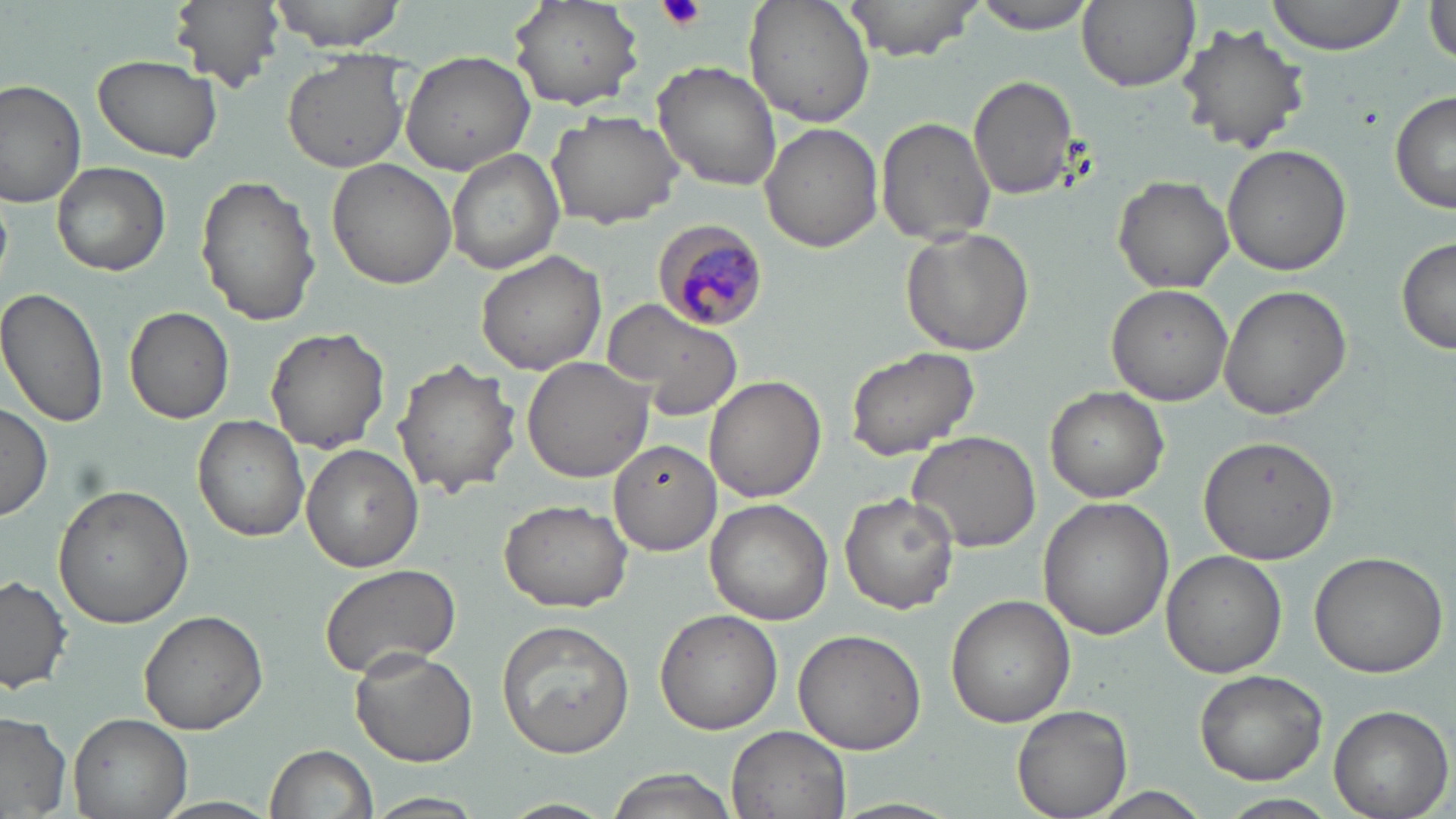

slide_level_diagnosis: Plasmodium malariae
stain: May-Grünwald-Giemsa
uninfected_red_blood_cell_locations: 'approximate bounding boxes as (x1, y1, x2, y2) in pixels: (171, 0, 285, 92), (266, 0, 413, 51), (510, 0, 645, 112), (742, 0, 876, 127), (841, 0, 987, 62), (969, 0, 1102, 35), (1077, 0, 1200, 92), (1265, 0, 1411, 55), (1424, 5, 1456, 66), (1176, 21, 1311, 152), (399, 48, 538, 175), (281, 49, 413, 173), (92, 53, 223, 162), (652, 61, 783, 191), (969, 74, 1081, 202), (0, 78, 89, 210), (1390, 90, 1456, 214), (545, 109, 683, 229), (875, 115, 996, 248), (760, 123, 884, 252), (1220, 145, 1353, 276), (445, 149, 564, 273), (327, 157, 459, 289), (51, 162, 170, 276), (195, 174, 321, 328), (1112, 176, 1234, 293), (902, 225, 1036, 356), (1397, 234, 1456, 358), (474, 248, 606, 375), (1218, 283, 1353, 418), (1105, 284, 1235, 404), (0, 285, 111, 432), (602, 297, 744, 421), (125, 306, 234, 424), (266, 325, 389, 453), (844, 345, 980, 461), (391, 358, 520, 499), (521, 358, 655, 482), (704, 376, 826, 503), (1044, 386, 1169, 502), (0, 400, 52, 523), (192, 415, 310, 542), (906, 430, 1041, 554), (1197, 432, 1340, 566), (610, 437, 722, 554), (300, 444, 423, 572), (53, 485, 193, 629), (839, 487, 961, 613), (1038, 497, 1173, 639), (499, 499, 632, 611), (705, 500, 834, 625), (1160, 549, 1288, 679), (1309, 549, 1450, 679), (318, 562, 462, 680), (0, 574, 73, 694), (947, 595, 1075, 727), (138, 609, 269, 735), (655, 609, 782, 735), (496, 619, 635, 760), (795, 628, 927, 754), (350, 647, 478, 767), (1194, 670, 1328, 785), (1011, 703, 1132, 819), (1329, 704, 1450, 818), (68, 711, 192, 819), (0, 712, 74, 819), (724, 725, 855, 819), (265, 744, 379, 819), (599, 769, 741, 819), (1085, 787, 1214, 819), (367, 792, 489, 818), (1219, 795, 1341, 819), (152, 797, 283, 819), (496, 799, 620, 819), (831, 800, 966, 819)'
image_size: 1456×819 pixels
field_of_view: one of a larger specimen
platelet_locations: 'approximate bounding boxes as (x1, y1, x2, y2) in pixels: (658, 0, 706, 32)'
preparation: thin blood smear
magnification: 1000x
modality: optical microscopy
plasmodium_malariae_infected_red_blood_cell_locations: 'approximate bounding boxes as (x1, y1, x2, y2) in pixels: (653, 219, 771, 330)'